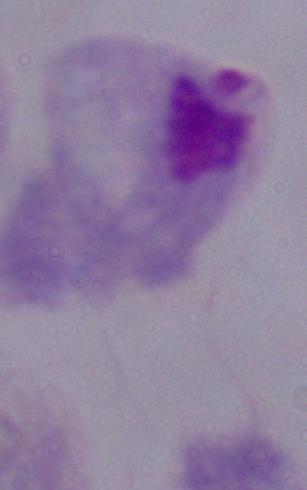
Captured at 1000x magnification. Photomicrograph. A trichomonad is seen.